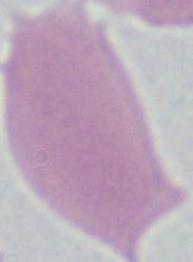
identification = red blood cell
magnification = 1000x
modality = photomicrograph